Outline platelets.
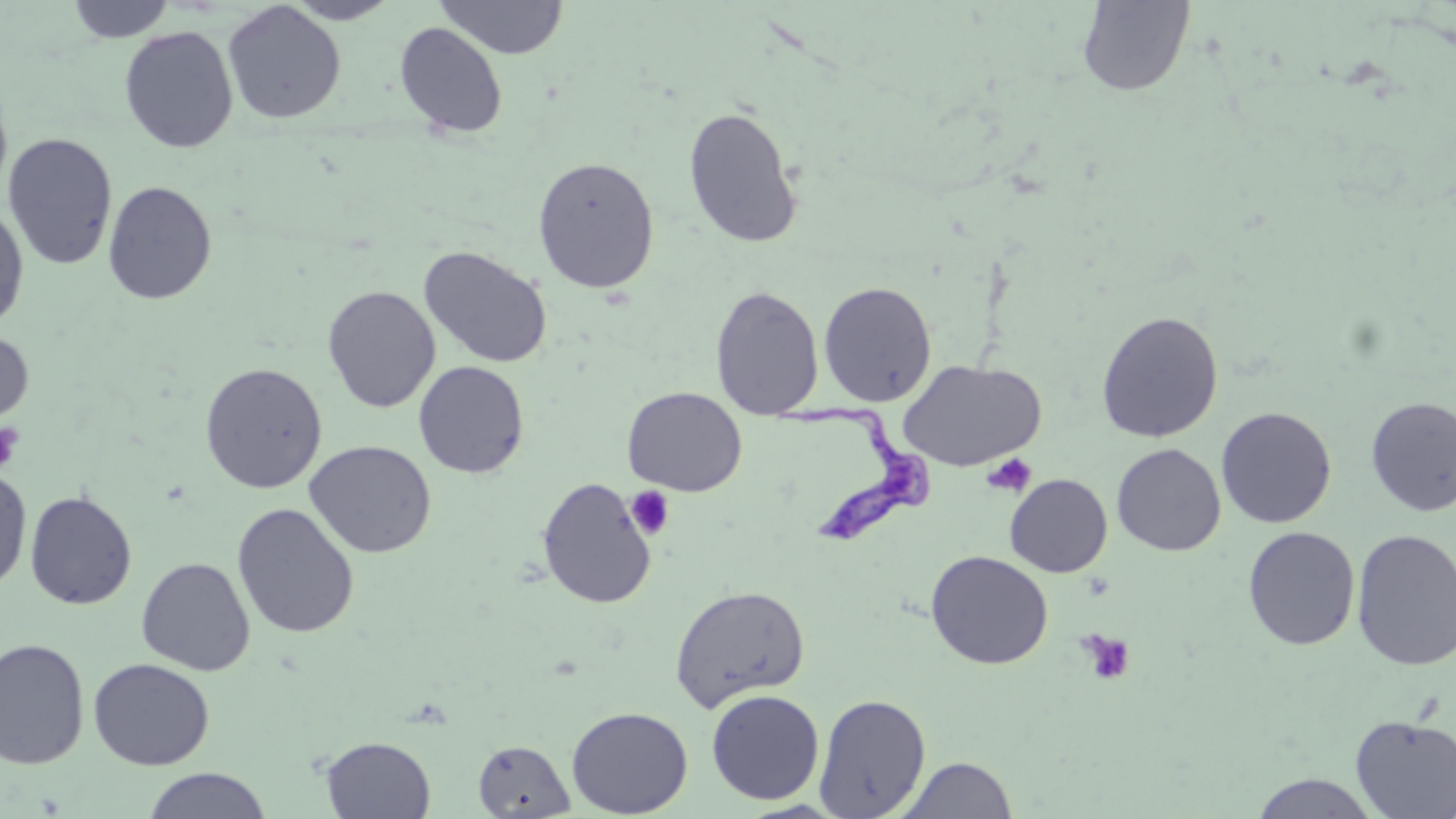

Approximate bounding boxes as [x1, y1, x2, y2] in pixels.
Platelets: [0, 421, 23, 473], [982, 454, 1036, 497], [626, 486, 676, 540], [1078, 630, 1136, 686].

Summary:
  - Uninfected red blood cell locations: [65, 0, 175, 43], [284, 0, 401, 25], [435, 0, 569, 59], [1076, 0, 1195, 96], [222, 2, 345, 124], [395, 22, 508, 139], [119, 26, 238, 153], [0, 78, 13, 202], [682, 105, 803, 248], [2, 132, 119, 271], [532, 156, 659, 294], [103, 180, 217, 305], [0, 201, 30, 333], [418, 245, 553, 369], [818, 280, 937, 407], [322, 285, 440, 413], [710, 285, 824, 419], [1096, 310, 1224, 443], [0, 328, 34, 430], [898, 359, 1046, 471], [413, 361, 530, 479], [199, 362, 327, 493], [622, 386, 747, 496], [1365, 396, 1456, 516], [1216, 406, 1337, 528], [1229, 409, 1340, 651], [304, 440, 436, 558], [1112, 443, 1226, 556], [0, 465, 32, 594], [1005, 473, 1113, 577], [536, 476, 657, 609], [24, 489, 137, 610], [232, 502, 359, 639], [1242, 526, 1360, 650], [1351, 528, 1456, 672], [925, 550, 1053, 669], [136, 557, 255, 675], [669, 584, 809, 712], [0, 637, 90, 770], [88, 657, 215, 770], [706, 688, 825, 805], [814, 692, 931, 817], [566, 705, 694, 818], [1350, 715, 1456, 817], [320, 736, 436, 818], [472, 739, 575, 817], [897, 756, 1018, 818], [141, 767, 273, 819], [1250, 772, 1379, 818]
  - Trypanosoma brucei locations: [777, 400, 940, 548]
  - Slide-level diagnosis: Trypanosoma brucei
  - Stain: May-Grünwald-Giemsa
  - Preparation: thin blood film
  - Image size: 1456×819 pixels
  - Magnification: 1000x
  - Field of view: single
  - Modality: optical microscopy